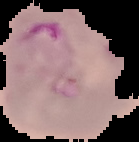
Summary:
  - Result: malaria parasites detected
  - Image size: 139×142 pixels
  - Image type: segmented cell region on a black background
  - Preparation: thin blood film